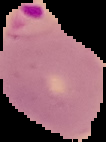
result = Plasmodium parasites detected
image type = segmented cell region with the area outside set to black
preparation = thin blood film
image size = 106×142 pixels